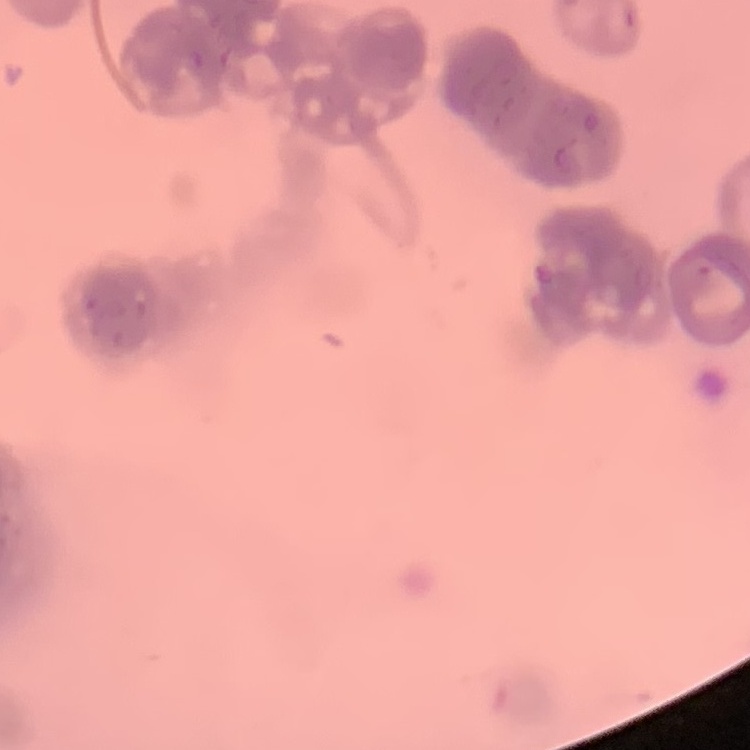 The red blood cells show rouleaux formation. Thin blood film. One tile cut from a larger photomicrograph. Field's or Giemsa stain.